Outline each blood parasite and name the species.
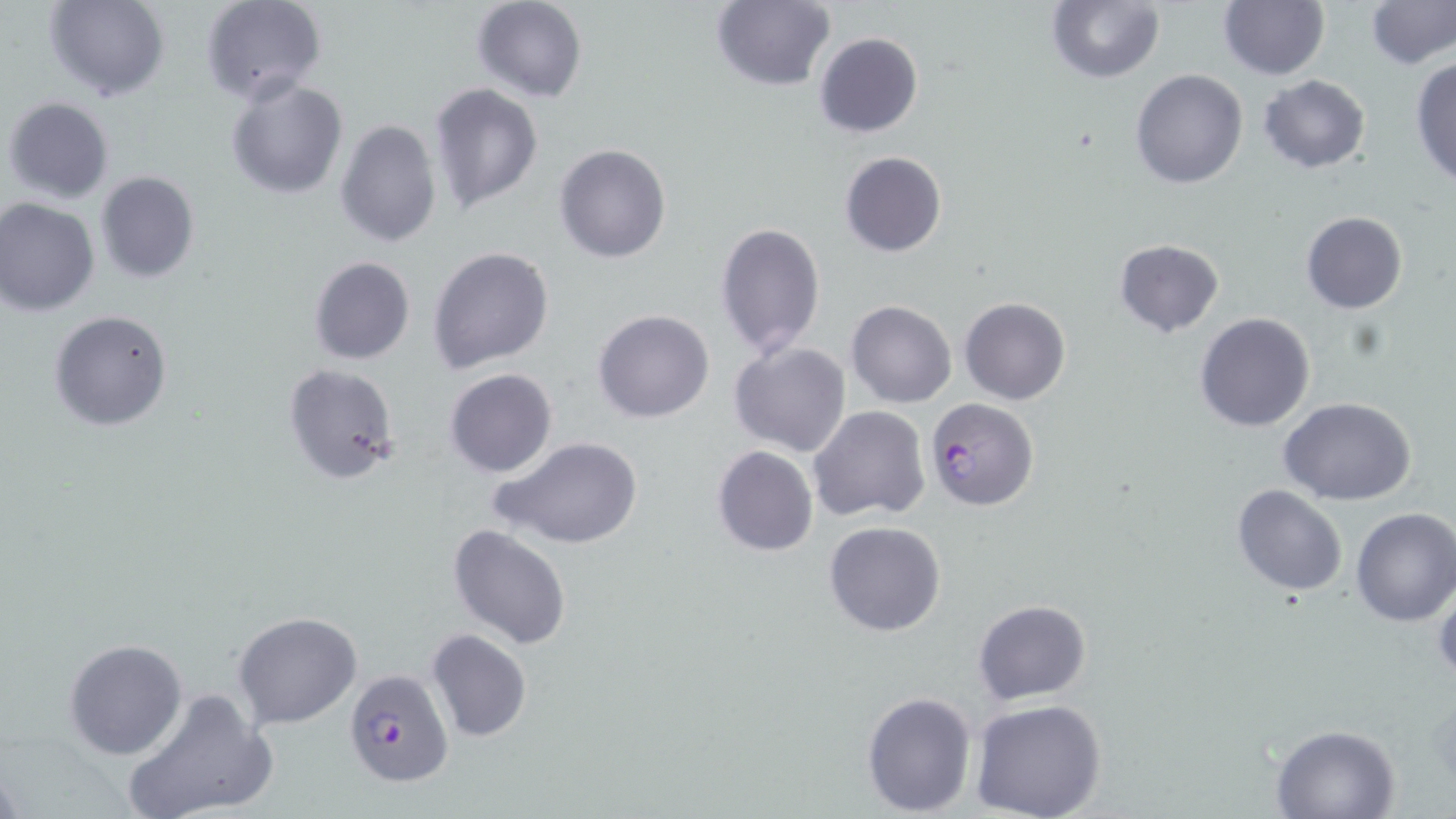
Approximate bounding boxes as (x1, y1, x2, y2) in pixels.
Plasmodium falciparum-infected red blood cells: (923, 397, 1038, 512), (343, 668, 452, 787).
No Plasmodium ovale, Plasmodium malariae, Plasmodium vivax, Babesia divergens, or Trypanosoma brucei observed.

Uninfected red blood cell locations: (44, 0, 168, 102), (203, 0, 326, 105), (470, 0, 589, 102), (710, 0, 835, 91), (1217, 0, 1329, 80), (1366, 0, 1455, 69), (1045, 1, 1164, 83), (814, 33, 923, 139), (1410, 56, 1456, 187), (1129, 68, 1249, 189), (1258, 74, 1371, 173), (224, 77, 349, 200), (428, 83, 543, 213), (4, 97, 114, 204), (334, 118, 443, 248), (554, 144, 672, 264), (838, 151, 947, 258), (94, 171, 200, 284), (0, 197, 100, 316), (1300, 211, 1407, 314), (716, 220, 826, 361), (1114, 237, 1225, 337), (428, 246, 554, 375), (308, 256, 416, 366), (960, 297, 1071, 405), (846, 299, 957, 408), (48, 309, 172, 432), (592, 311, 714, 424), (1194, 313, 1315, 432), (728, 340, 852, 459), (283, 362, 401, 485), (444, 368, 559, 478), (1279, 397, 1418, 504), (809, 405, 930, 521), (492, 436, 642, 550), (711, 445, 818, 558), (1231, 485, 1347, 597), (1350, 507, 1456, 626), (824, 521, 947, 636), (447, 522, 574, 649), (1432, 575, 1456, 682), (973, 599, 1091, 704), (233, 609, 363, 729), (426, 630, 532, 744), (63, 638, 188, 760), (120, 689, 278, 819), (862, 690, 977, 813), (968, 698, 1108, 819), (1269, 723, 1400, 817). Slide-level diagnosis: Plasmodium falciparum. Thin blood smear. 1000x magnification. Optical microscopy. May-Grünwald-Giemsa-stained preparation. Image is 1456×819 pixels. One field of a larger specimen.